Assess this cell for malaria.
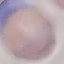

It is uninfected.

Summary:
  - Capture: smartphone camera at the microscope eyepiece
  - Image type: cell patch, automatically extracted from a larger field of view and resized to 64 × 64 pixels
  - Stain: Giemsa
  - Preparation: thin blood smear